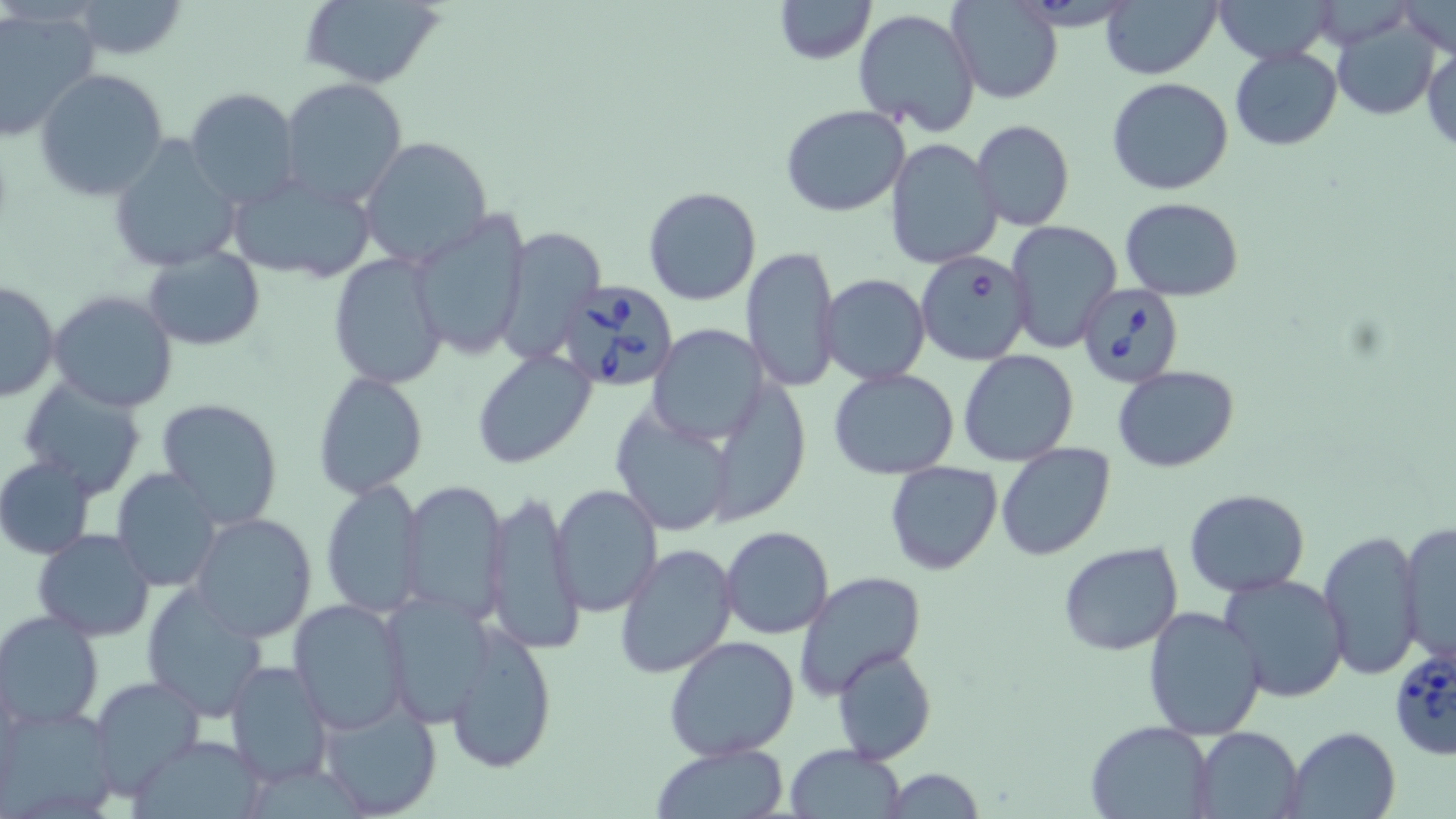
Approximate bounding boxes as named x1/y1/x2/y2 corners in pixels. Babesia divergens-infected red blood cell locations: (x1=915, y1=251, x2=1033, y2=366), (x1=552, y1=279, x2=681, y2=393), (x1=1079, y1=282, x2=1185, y2=388), (x1=1389, y1=644, x2=1456, y2=764). Uninfected red blood cell locations: (x1=299, y1=0, x2=448, y2=89), (x1=772, y1=0, x2=876, y2=64), (x1=1099, y1=0, x2=1221, y2=81), (x1=1212, y1=0, x2=1338, y2=64), (x1=63, y1=1, x2=188, y2=60), (x1=947, y1=2, x2=1062, y2=105), (x1=1397, y1=3, x2=1453, y2=59), (x1=0, y1=7, x2=101, y2=142), (x1=853, y1=8, x2=981, y2=134), (x1=1332, y1=16, x2=1443, y2=119), (x1=1423, y1=43, x2=1455, y2=152), (x1=1229, y1=46, x2=1343, y2=150), (x1=34, y1=67, x2=170, y2=201), (x1=1106, y1=77, x2=1234, y2=195), (x1=279, y1=78, x2=409, y2=210), (x1=184, y1=86, x2=301, y2=209), (x1=781, y1=104, x2=911, y2=216), (x1=971, y1=120, x2=1074, y2=231), (x1=106, y1=136, x2=240, y2=274), (x1=360, y1=137, x2=493, y2=269), (x1=884, y1=139, x2=1003, y2=269), (x1=225, y1=171, x2=378, y2=285), (x1=643, y1=186, x2=762, y2=305), (x1=1120, y1=197, x2=1243, y2=302), (x1=406, y1=209, x2=530, y2=361), (x1=1006, y1=219, x2=1121, y2=353), (x1=494, y1=226, x2=606, y2=363), (x1=741, y1=245, x2=842, y2=392), (x1=143, y1=246, x2=264, y2=350), (x1=330, y1=252, x2=449, y2=392), (x1=820, y1=274, x2=931, y2=386), (x1=1, y1=281, x2=60, y2=404), (x1=48, y1=290, x2=179, y2=412), (x1=647, y1=324, x2=770, y2=446), (x1=959, y1=347, x2=1079, y2=466), (x1=472, y1=348, x2=598, y2=470), (x1=1111, y1=365, x2=1241, y2=472), (x1=828, y1=367, x2=960, y2=480), (x1=313, y1=373, x2=428, y2=497), (x1=17, y1=377, x2=147, y2=497), (x1=157, y1=397, x2=285, y2=528), (x1=609, y1=408, x2=738, y2=537), (x1=995, y1=442, x2=1116, y2=561), (x1=0, y1=456, x2=97, y2=560), (x1=885, y1=460, x2=1004, y2=576), (x1=111, y1=469, x2=225, y2=592), (x1=400, y1=477, x2=510, y2=625), (x1=320, y1=479, x2=423, y2=617), (x1=550, y1=484, x2=663, y2=616), (x1=1184, y1=488, x2=1311, y2=597), (x1=482, y1=491, x2=582, y2=655), (x1=189, y1=513, x2=319, y2=643), (x1=1397, y1=521, x2=1456, y2=669), (x1=721, y1=526, x2=833, y2=639), (x1=33, y1=528, x2=157, y2=641), (x1=1317, y1=530, x2=1425, y2=680), (x1=1058, y1=541, x2=1184, y2=655), (x1=614, y1=544, x2=738, y2=679), (x1=794, y1=571, x2=927, y2=696), (x1=1218, y1=573, x2=1349, y2=702), (x1=141, y1=582, x2=271, y2=722), (x1=379, y1=589, x2=501, y2=727), (x1=288, y1=598, x2=410, y2=734), (x1=1141, y1=605, x2=1267, y2=741), (x1=0, y1=612, x2=104, y2=730), (x1=444, y1=626, x2=559, y2=776), (x1=663, y1=635, x2=800, y2=760), (x1=831, y1=646, x2=937, y2=765), (x1=225, y1=661, x2=334, y2=787), (x1=86, y1=672, x2=206, y2=797), (x1=318, y1=697, x2=443, y2=817), (x1=0, y1=704, x2=120, y2=817), (x1=1086, y1=720, x2=1212, y2=818), (x1=1282, y1=726, x2=1402, y2=819), (x1=1192, y1=727, x2=1302, y2=817), (x1=131, y1=733, x2=264, y2=817), (x1=650, y1=743, x2=789, y2=819), (x1=784, y1=744, x2=907, y2=819), (x1=879, y1=767, x2=986, y2=819). Slide-level diagnosis: Babesia divergens. Thin blood film. Image is 1456×819 pixels. 1000x magnification. One field of a larger specimen. May-Grünwald-Giemsa-stained preparation. Light microscopy.